Comment on the morphology of the erythrocytes.
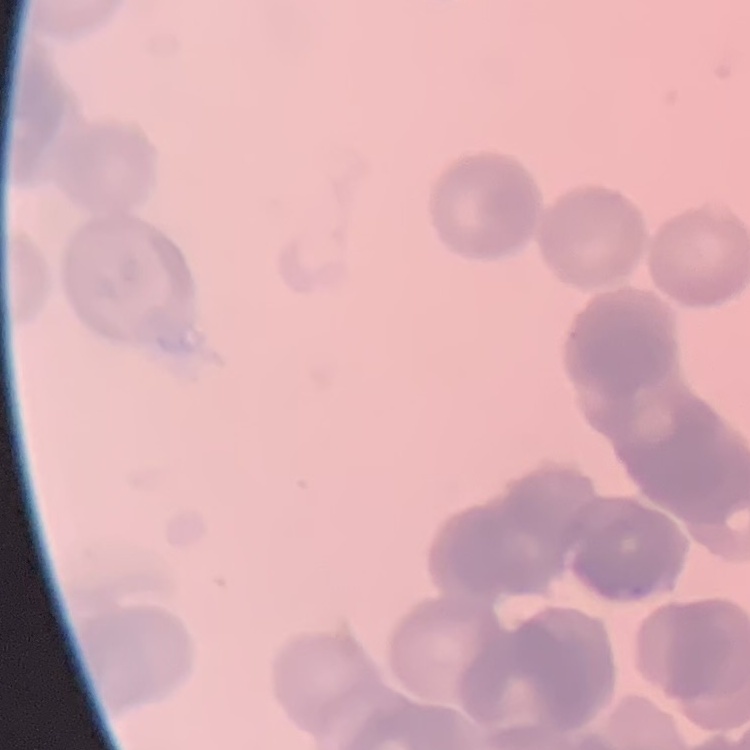
They show rouleaux formation.

Thin peripheral smear. Square crop of a larger photomicrograph. Field's or Giemsa stain.